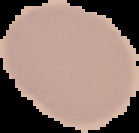

{
  "image_type": "segmented cell region on a black background",
  "preparation": "thin blood smear",
  "image_size": "139×133 pixels",
  "malaria_status": "uninfected"
}